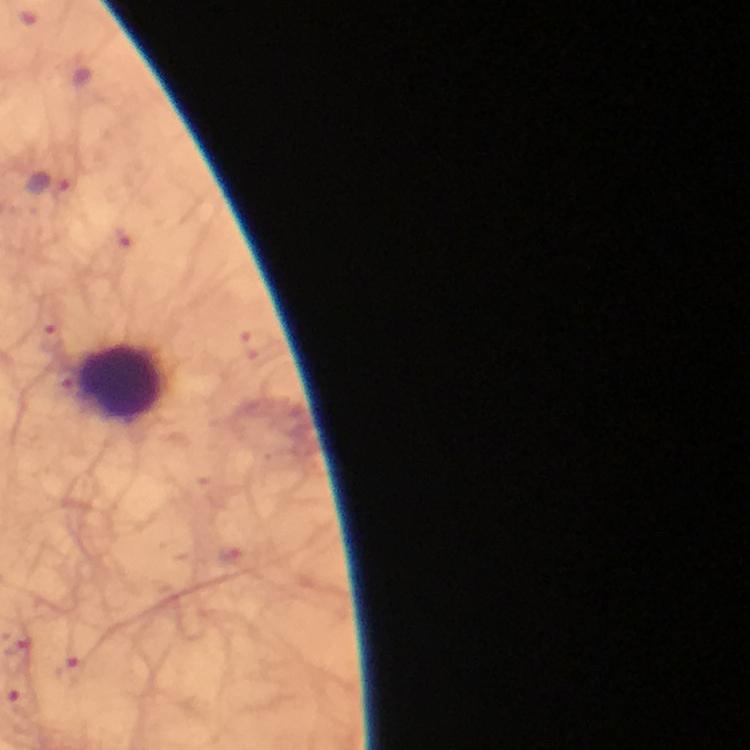

Approximate centers as (x, y) in pixels. Plasmodium parasite locations: (50, 184). Leukocyte locations: (120, 379). Giemsa stain. Thick blood smear. Immersion oil was used. A crop from one field of view. Smartphone photograph taken through a microscope. Image is 750×750 pixels. At 100x magnification. From a diagnostic examination for malaria.